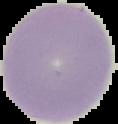
Result: no malaria parasites detected. Segmented cell region on a black background. Image is 118×124 pixels. From a thin blood film.